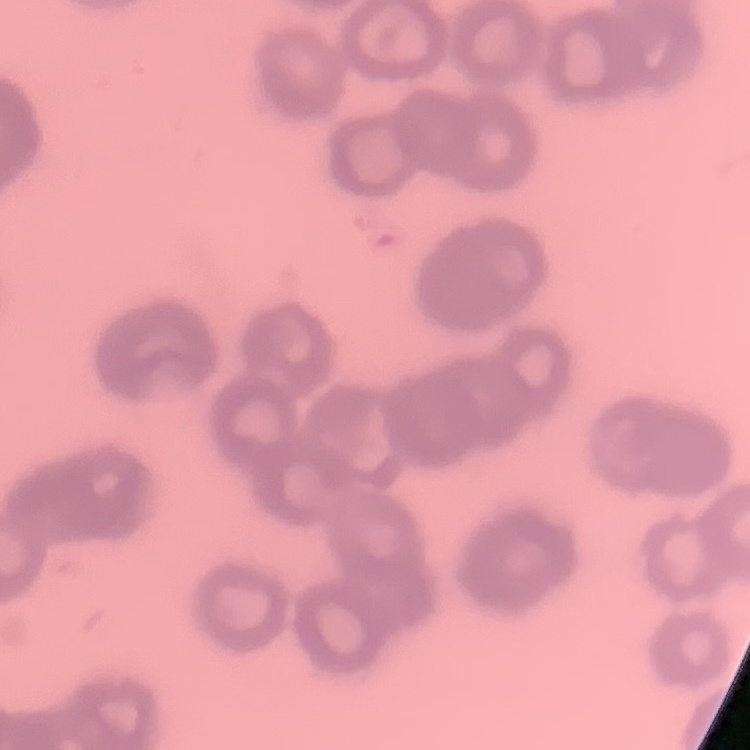
red blood cell morphology = rouleaux formation
stain = Field's or Giemsa
preparation = thin blood smear
image type = one tile cut from a larger photomicrograph